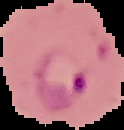

{
  "image_type": "cell region segmented out of the field of view; surrounding area masked to black",
  "image_size": "124×130 pixels",
  "preparation": "thin blood smear",
  "malaria_status": "parasitized"
}